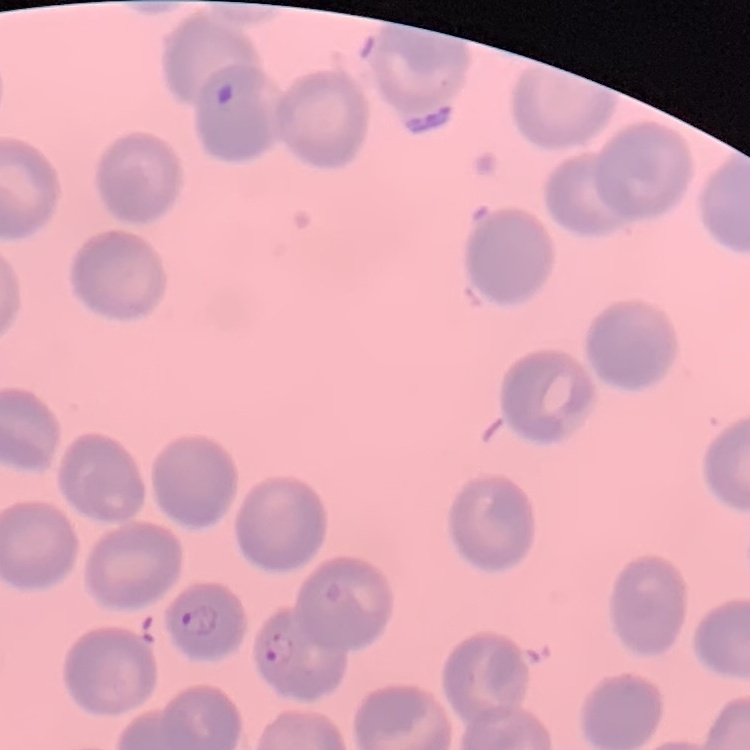

Summary:
  - Red blood cell morphology: no rouleaux formation
  - Preparation: thin blood film
  - Image type: square crop of a larger photomicrograph
  - Stain: Field's or Giemsa